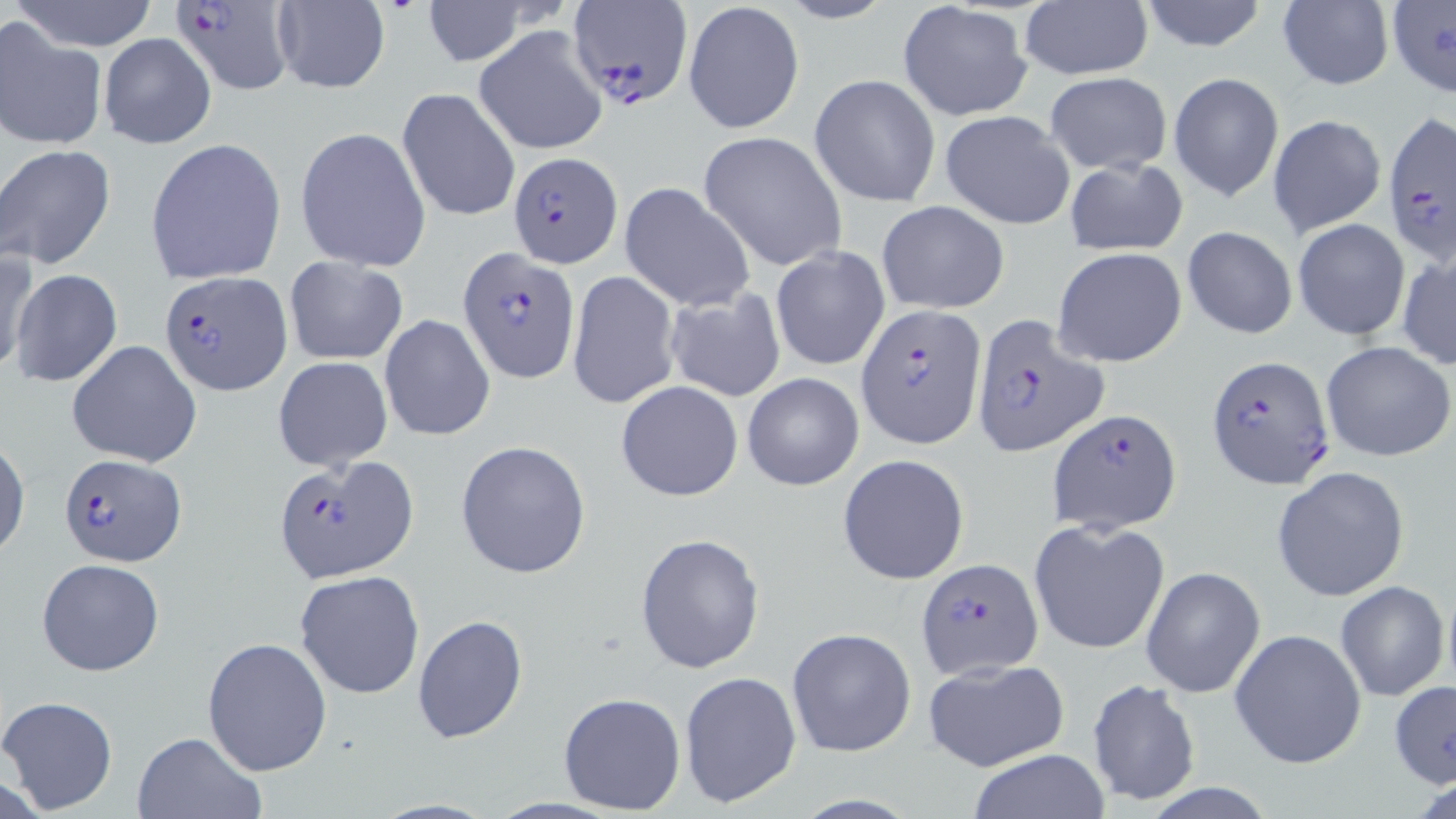
Approximate bounding boxes as named x1/y1/x2/y2 corners in pixels. Uninfected red blood cell locations: (x1=6, y1=0, x2=163, y2=52), (x1=420, y1=0, x2=533, y2=64), (x1=771, y1=0, x2=897, y2=25), (x1=1135, y1=0, x2=1271, y2=52), (x1=270, y1=1, x2=389, y2=94), (x1=898, y1=2, x2=1034, y2=123), (x1=1275, y1=2, x2=1394, y2=90), (x1=1385, y1=2, x2=1456, y2=100), (x1=685, y1=3, x2=803, y2=132), (x1=1019, y1=3, x2=1152, y2=80), (x1=0, y1=19, x2=104, y2=149), (x1=474, y1=25, x2=609, y2=155), (x1=97, y1=32, x2=216, y2=149), (x1=1044, y1=73, x2=1172, y2=173), (x1=1169, y1=73, x2=1286, y2=202), (x1=810, y1=74, x2=940, y2=207), (x1=397, y1=86, x2=521, y2=223), (x1=940, y1=110, x2=1076, y2=231), (x1=1267, y1=114, x2=1386, y2=239), (x1=296, y1=127, x2=431, y2=270), (x1=697, y1=130, x2=847, y2=272), (x1=145, y1=137, x2=288, y2=285), (x1=2, y1=145, x2=116, y2=269), (x1=1062, y1=156, x2=1189, y2=257), (x1=619, y1=181, x2=756, y2=314), (x1=876, y1=199, x2=1010, y2=314), (x1=1292, y1=218, x2=1411, y2=342), (x1=1182, y1=226, x2=1298, y2=341), (x1=770, y1=247, x2=890, y2=372), (x1=1051, y1=247, x2=1188, y2=369), (x1=1397, y1=249, x2=1456, y2=371), (x1=0, y1=250, x2=39, y2=376), (x1=284, y1=257, x2=408, y2=364), (x1=11, y1=270, x2=123, y2=385), (x1=566, y1=271, x2=680, y2=409), (x1=662, y1=289, x2=787, y2=403), (x1=378, y1=314, x2=496, y2=441), (x1=67, y1=340, x2=203, y2=467), (x1=1322, y1=340, x2=1455, y2=462), (x1=273, y1=357, x2=393, y2=471), (x1=743, y1=372, x2=863, y2=491), (x1=615, y1=381, x2=744, y2=501), (x1=0, y1=439, x2=29, y2=561), (x1=455, y1=440, x2=591, y2=580), (x1=837, y1=454, x2=970, y2=585), (x1=1271, y1=466, x2=1410, y2=602), (x1=1029, y1=519, x2=1170, y2=655), (x1=635, y1=532, x2=766, y2=674), (x1=36, y1=558, x2=166, y2=676), (x1=1141, y1=566, x2=1264, y2=698), (x1=295, y1=570, x2=424, y2=700), (x1=1335, y1=581, x2=1449, y2=702), (x1=412, y1=613, x2=528, y2=743), (x1=786, y1=627, x2=915, y2=759), (x1=1229, y1=628, x2=1368, y2=769), (x1=202, y1=637, x2=332, y2=775), (x1=921, y1=657, x2=1070, y2=773), (x1=678, y1=671, x2=801, y2=807), (x1=1087, y1=680, x2=1201, y2=806), (x1=1389, y1=681, x2=1456, y2=791), (x1=557, y1=691, x2=687, y2=816), (x1=0, y1=695, x2=118, y2=813), (x1=133, y1=730, x2=265, y2=818), (x1=967, y1=750, x2=1110, y2=819). Plasmodium falciparum-infected red blood cell locations: (x1=171, y1=0, x2=297, y2=95), (x1=567, y1=3, x2=693, y2=109), (x1=1379, y1=113, x2=1454, y2=261), (x1=509, y1=150, x2=621, y2=267), (x1=457, y1=246, x2=579, y2=380), (x1=160, y1=272, x2=292, y2=394), (x1=859, y1=305, x2=987, y2=447), (x1=970, y1=315, x2=1108, y2=457), (x1=1207, y1=355, x2=1334, y2=490), (x1=1047, y1=408, x2=1181, y2=534), (x1=57, y1=454, x2=186, y2=566), (x1=273, y1=456, x2=417, y2=583), (x1=915, y1=557, x2=1044, y2=681). Slide-level diagnosis: Plasmodium falciparum. One field of a larger specimen. 1000x magnification. Light microscopy. May-Grünwald-Giemsa-stained preparation. Image is 1456×819 pixels. Thin blood film.